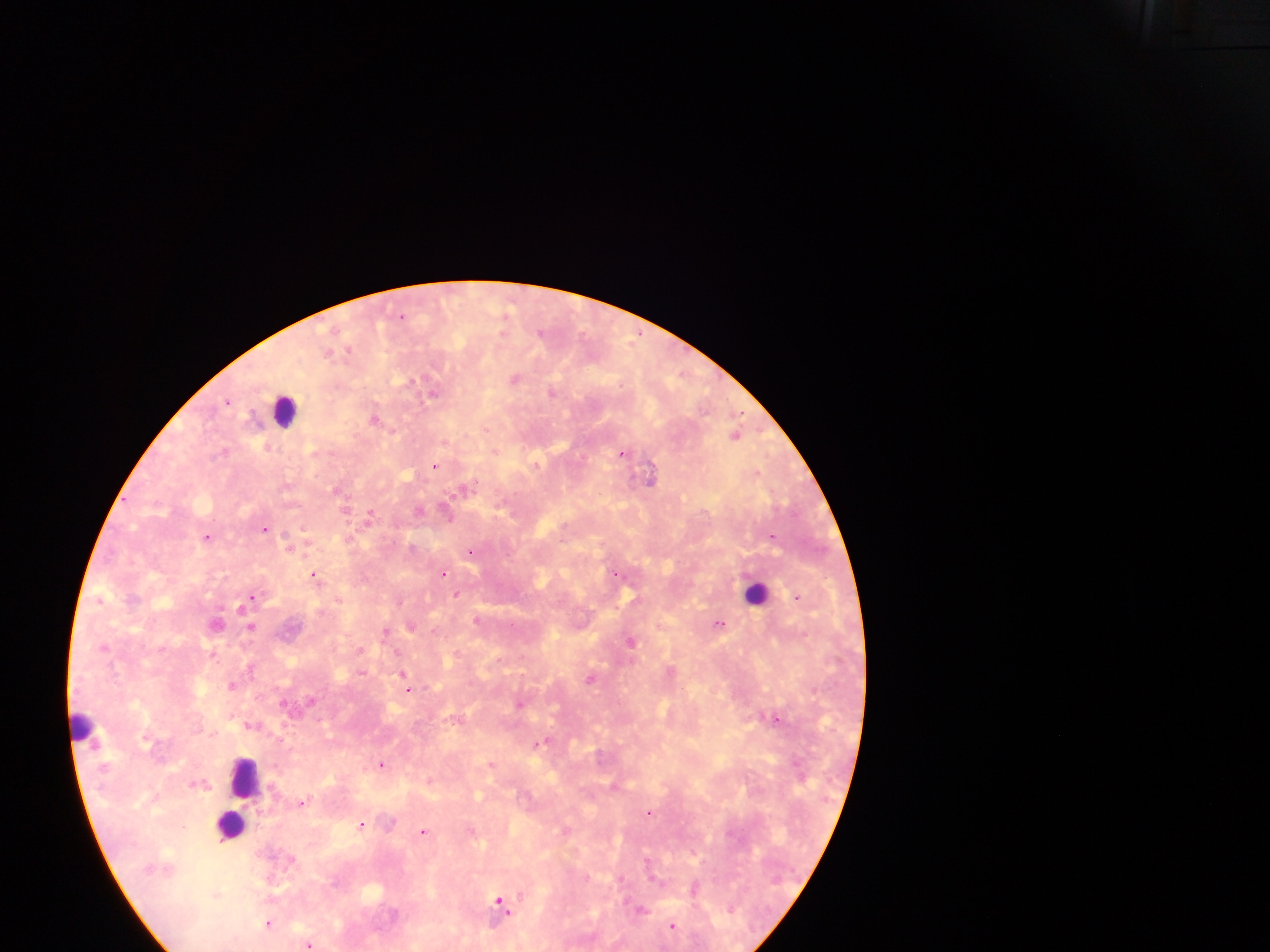
preparation = thick blood smear
capture = mobile-phone photograph through a microscope
country = Ghana
leukocyte locations = approximate centers as x y in pixels: 285 410; 757 592; 82 725; 244 777; 238 808; 230 825
malaria parasite locations = approximate centers as x y in pixels: 507 312; 402 315; 541 332; 349 350; 328 353; 515 378; 411 381; 552 392; 434 394; 228 402; 375 418; 736 433; 445 441; 223 451; 495 451; 623 453; 435 465; 651 477; 467 486; 419 511; 448 515; 370 516; 265 529; 207 537; 773 537; 412 546; 289 547; 471 551; 443 573; 617 573; 315 575; 457 594; 797 596; 252 597; 100 600; 243 607; 477 619; 216 622; 719 623; 251 626; 412 626; 386 631; 631 641; 104 647; 214 653; 398 653; 250 667; 361 672; 591 678; 405 681; 231 685; 407 689; 520 704; 777 718; 541 743; 382 764; 492 764; 428 781; 303 803; 650 812; 362 824; 566 829; 423 831; 695 888; 500 902; 641 909; 268 923; 673 925; 310 944
field of view = single
image size = 1270×952 pixels